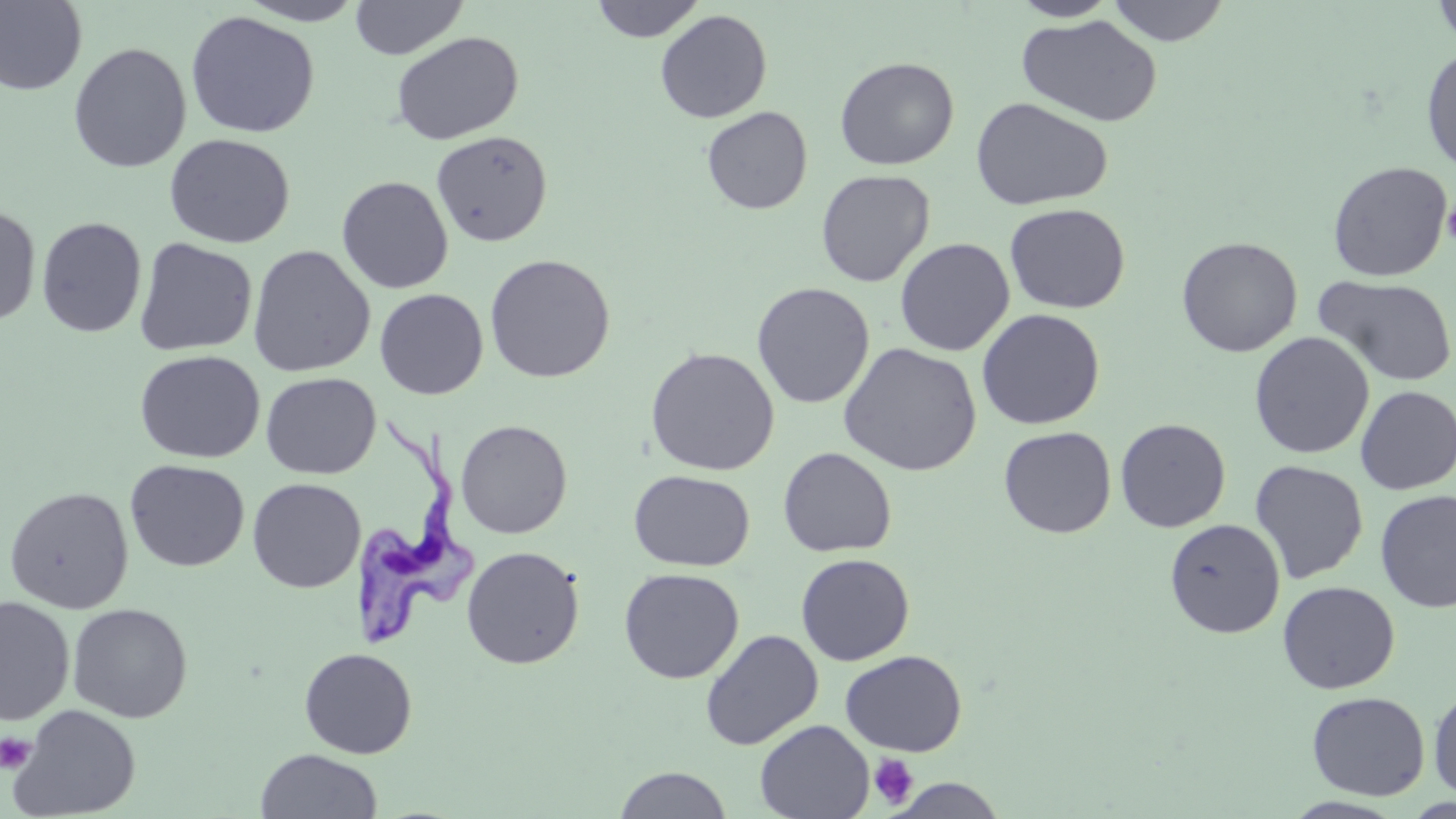
{
  "slide_level_diagnosis": "Trypanosoma brucei",
  "magnification": "1000x",
  "platelet_locations": "approximate bounding boxes as (x1,y1)-(x2,y2) corner pairs in pixels: (1442,199)-(1456,246), (0,733)-(35,773), (868,753)-(919,809)",
  "stain": "May-Grünwald-Giemsa",
  "modality": "optical microscopy",
  "trypanosoma_brucei_locations": "approximate bounding boxes as (x1,y1)-(x2,y2) corner pairs in pixels: (349,413)-(477,653)",
  "field_of_view": "one of a larger specimen",
  "preparation": "thin blood film",
  "uninfected_red_blood_cell_locations": "approximate bounding boxes as (x1,y1)-(x2,y2) corner pairs in pixels: (236,0)-(367,26), (349,0)-(468,60), (590,0)-(706,42), (1105,0)-(1232,46), (1432,0)-(1456,50), (0,1)-(88,96), (1008,1)-(1121,22), (654,9)-(773,123), (184,10)-(321,138), (1017,13)-(1162,127), (391,31)-(524,145), (67,42)-(192,173), (1421,45)-(1456,176), (834,56)-(959,171), (970,96)-(1113,211), (701,106)-(813,215), (431,130)-(553,247), (164,133)-(295,249), (1327,160)-(1453,281), (815,169)-(936,288), (336,176)-(454,294), (1004,203)-(1130,314), (0,204)-(41,328), (36,216)-(147,338), (1176,236)-(1303,358), (133,237)-(258,356), (894,237)-(1015,357), (247,244)-(376,378), (484,254)-(615,383), (1314,274)-(1456,387), (751,281)-(875,409), (374,288)-(489,400), (976,308)-(1105,430), (1249,331)-(1375,459), (837,341)-(982,476), (644,347)-(780,476), (134,350)-(265,464), (260,372)-(381,479), (1355,385)-(1456,495), (1114,418)-(1231,532), (455,419)-(573,539), (998,425)-(1116,538), (777,447)-(897,558), (125,459)-(250,572), (1249,459)-(1369,584), (629,470)-(754,571), (247,478)-(366,593), (3,486)-(134,614), (1375,489)-(1456,613), (1164,518)-(1286,638), (462,546)-(584,669), (795,553)-(915,666), (618,567)-(744,684), (1277,580)-(1400,694), (0,596)-(75,726), (67,603)-(192,723), (700,629)-(823,750), (299,647)-(418,759), (840,650)-(967,756), (1428,686)-(1456,800), (1306,690)-(1430,801), (8,704)-(142,818), (754,719)-(874,819), (254,748)-(383,819), (613,766)-(733,818), (886,777)-(1009,818)",
  "image_size": "1456×819 pixels"
}